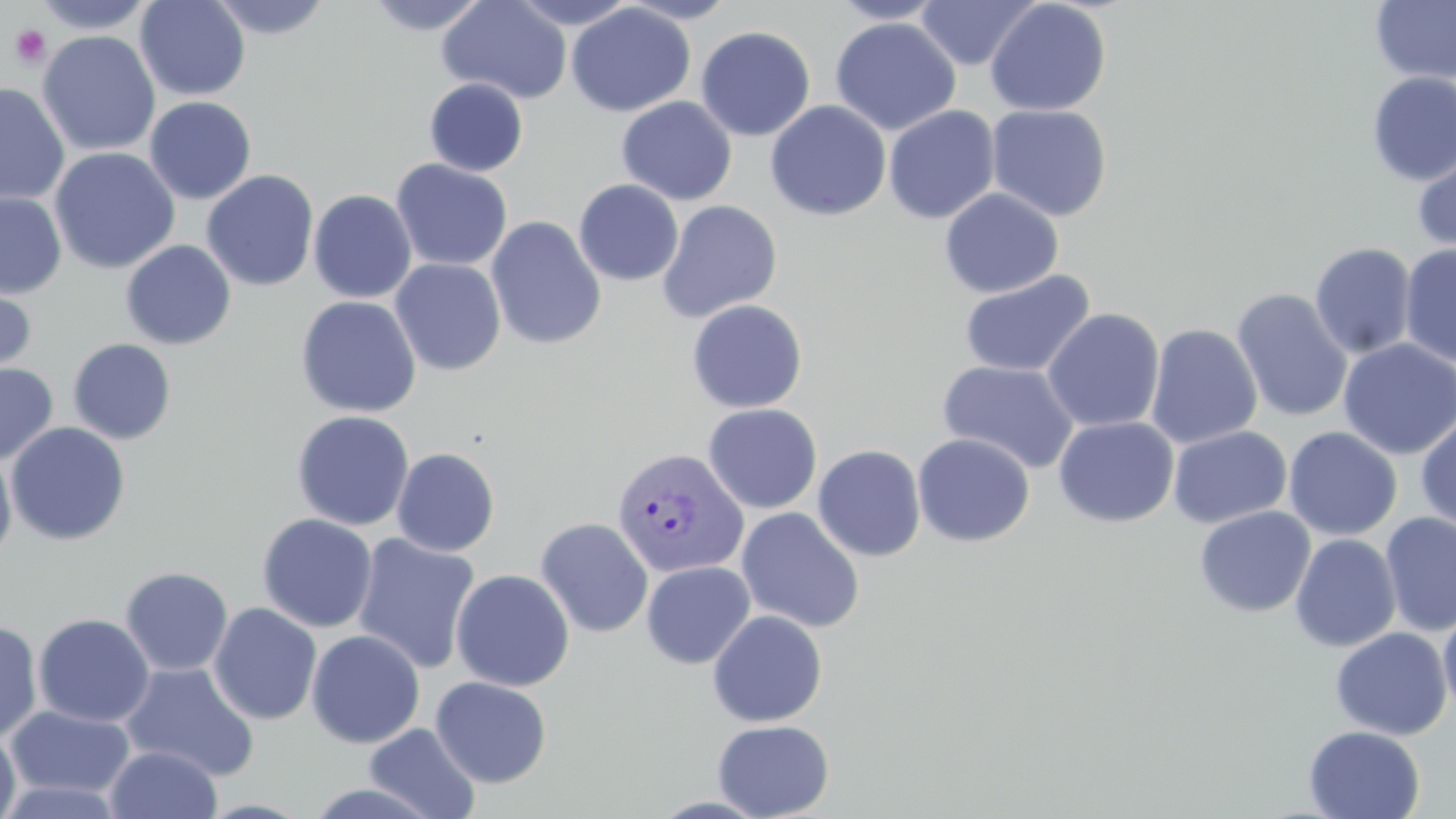
Approximate bounding boxes as (x1,y1)-(x2,y2) corner pairs in pixels. Uninfected red blood cell locations: (31,0)-(157,34), (136,0)-(250,101), (206,0)-(334,40), (365,0)-(491,35), (437,0)-(572,104), (618,0)-(739,23), (828,0)-(949,24), (914,0)-(1041,70), (1370,0)-(1456,84), (506,1)-(641,29), (985,1)-(1112,116), (566,3)-(696,117), (829,17)-(960,136), (695,25)-(816,141), (37,30)-(160,157), (1366,72)-(1456,186), (424,78)-(529,176), (0,83)-(69,204), (144,96)-(257,205), (616,96)-(737,205), (765,100)-(892,221), (986,104)-(1114,221), (883,105)-(1001,224), (49,147)-(180,274), (1412,147)-(1456,257), (391,158)-(513,271), (202,170)-(319,291), (573,179)-(684,286), (939,188)-(1064,298), (308,189)-(417,303), (0,191)-(67,299), (657,200)-(783,323), (486,216)-(607,351), (120,240)-(236,350), (1310,242)-(1417,360), (1399,244)-(1456,367), (390,258)-(506,375), (958,269)-(1096,378), (0,276)-(37,384), (1230,288)-(1353,422), (295,296)-(422,417), (685,299)-(808,413), (1042,308)-(1165,432), (1145,323)-(1263,449), (1337,337)-(1456,459), (67,338)-(177,444), (938,360)-(1081,474), (0,362)-(58,465), (702,403)-(822,515), (291,410)-(415,531), (1415,411)-(1456,534), (1053,416)-(1179,527), (5,422)-(131,546), (1168,425)-(1292,528), (1283,426)-(1402,541), (912,433)-(1036,547), (812,444)-(927,561), (392,447)-(500,557), (0,450)-(17,563), (1193,506)-(1316,618), (736,507)-(865,633), (1380,512)-(1456,636), (257,513)-(377,633), (535,516)-(653,638), (1290,533)-(1401,652), (352,534)-(481,674), (233,542)-(365,683), (641,561)-(756,669), (119,566)-(234,676), (450,569)-(574,691), (208,603)-(322,725), (1438,605)-(1456,720), (707,610)-(827,727), (32,613)-(155,727), (0,620)-(42,743), (1330,627)-(1452,740), (306,629)-(425,748), (120,661)-(260,781), (430,676)-(552,788), (4,705)-(136,800), (712,719)-(835,819), (363,723)-(481,818), (1304,725)-(1425,818), (0,728)-(21,819), (105,745)-(222,818), (0,777)-(127,818), (304,782)-(444,818). Platelet locations: (10,25)-(52,69). Plasmodium vivax-infected red blood cell locations: (611,447)-(749,580). Slide-level diagnosis: Plasmodium vivax. Thin blood smear. May-Grünwald-Giemsa-stained preparation. Light microscopy. Image is 1456×819 pixels. Captured at 1000x magnification. One field of a larger specimen.